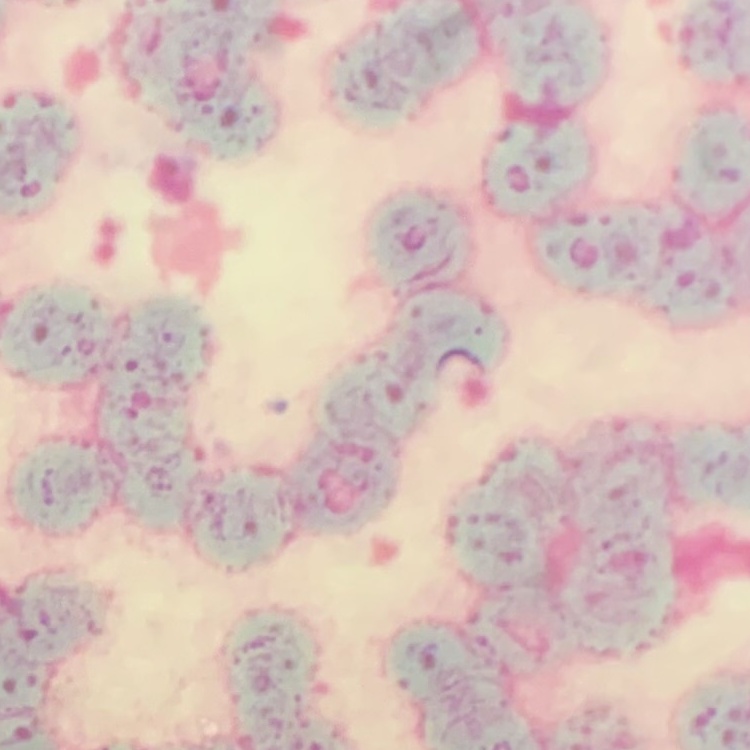 The red blood cells show rouleaux formation. Thin blood film. One tile cut from a larger photomicrograph. Stained with either Field's or Giemsa.